Give the position of every leukocyte visible.
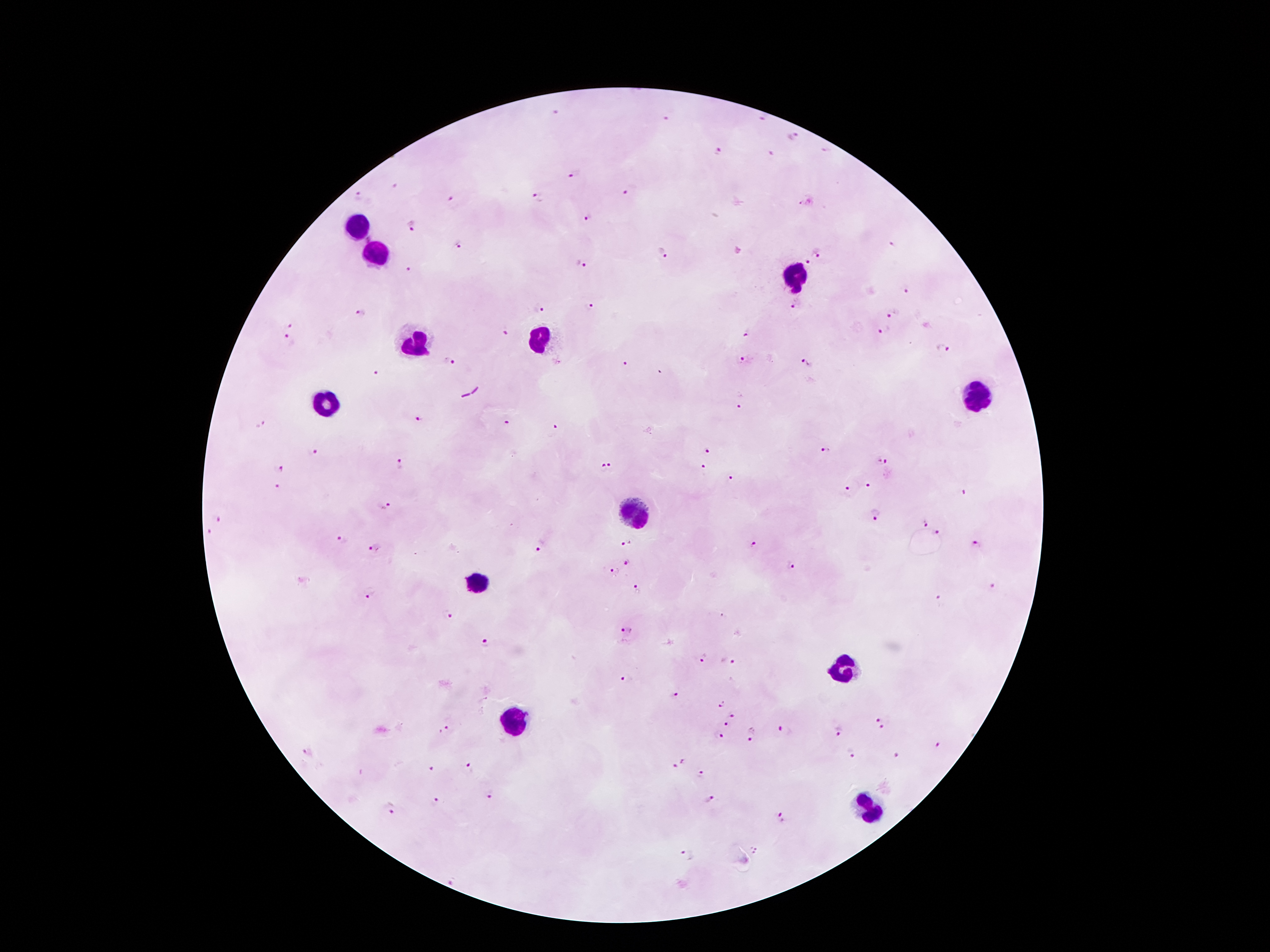
Approximate centers as {x, y} in pixels.
Leukocytes: {360, 228}, {374, 254}, {797, 276}, {540, 338}, {414, 343}, {981, 394}, {326, 403}, {637, 511}, {477, 585}, {843, 670}, {515, 723}, {872, 807}.

{
  "patient_malaria_status": "positive for Plasmodium falciparum",
  "magnification": "100x",
  "preparation": "thick peripheral-blood smear",
  "capture": "smartphone camera through the microscope eyepiece",
  "image_size": "1270×952 pixels",
  "field_of_view": "one from this slide",
  "stain": "Giemsa",
  "malaria_parasite_locations": "approximate centers as {x, y} in pixels: {667, 116}, {763, 118}, {792, 135}, {825, 149}, {720, 150}, {574, 175}, {626, 189}, {358, 196}, {538, 197}, {450, 204}, {800, 205}, {587, 218}, {412, 225}, {890, 244}, {460, 245}, {664, 251}, {819, 252}, {810, 263}, {581, 264}, {409, 269}, {906, 290}, {796, 305}, {590, 306}, {539, 307}, {359, 314}, {893, 314}, {287, 325}, {885, 329}, {505, 331}, {747, 332}, {288, 338}, {943, 348}, {745, 360}, {449, 362}, {805, 362}, {626, 364}, {378, 374}, {739, 408}, {418, 418}, {507, 422}, {260, 423}, {556, 427}, {825, 449}, {313, 452}, {709, 452}, {881, 461}, {400, 465}, {612, 465}, {280, 468}, {704, 468}, {603, 469}, {732, 482}, {869, 484}, {277, 487}, {847, 490}, {965, 491}, {386, 505}, {875, 514}, {218, 520}, {924, 522}, {210, 532}, {938, 533}, {342, 540}, {627, 543}, {752, 544}, {977, 545}, {374, 548}, {539, 548}, {628, 563}, {790, 566}, {615, 571}, {992, 587}, {636, 589}, {368, 594}, {939, 600}, {447, 613}, {626, 630}, {483, 641}, {704, 656}, {727, 663}, {626, 679}, {674, 695}, {721, 704}, {732, 715}, {882, 718}, {727, 724}, {885, 727}, {445, 729}, {785, 730}, {838, 730}, {718, 734}, {750, 735}, {936, 746}, {307, 753}, {850, 753}, {898, 756}, {677, 762}, {470, 765}, {429, 769}, {701, 776}, {489, 794}, {437, 801}, {709, 801}, {391, 809}, {779, 820}, {756, 851}, {686, 855}"
}